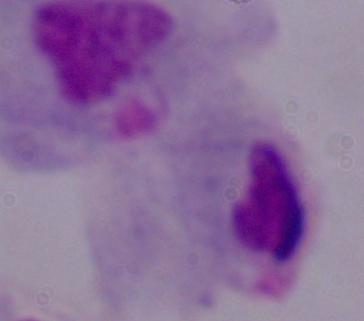
Summary:
  - Identification: trichomonad
  - Modality: micrograph
  - Magnification: 1000x